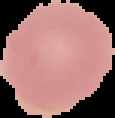
malaria status = uninfected
preparation = thin blood smear
image size = 115×118 pixels
image type = segmented cell region on a black background